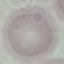
result = no malaria parasites seen
preparation = thin blood smear
stain = Giemsa
capture = smartphone camera at the microscope eyepiece
image type = cell patch, automatically extracted from a larger field of view and resized to 64 × 64 pixels